Classify this cell by malaria status.
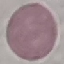
Uninfected.

Summary:
  - Capture: smartphone through the microscope eyepiece
  - Preparation: thin blood film
  - Stain: Giemsa
  - Image type: automatically extracted cell patch, resized to 64 × 64 pixels